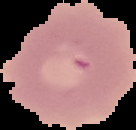
Summary:
  - Malaria status: uninfected
  - Image type: segmented cell region with the area outside set to black
  - Preparation: thin blood film
  - Image size: 136×130 pixels